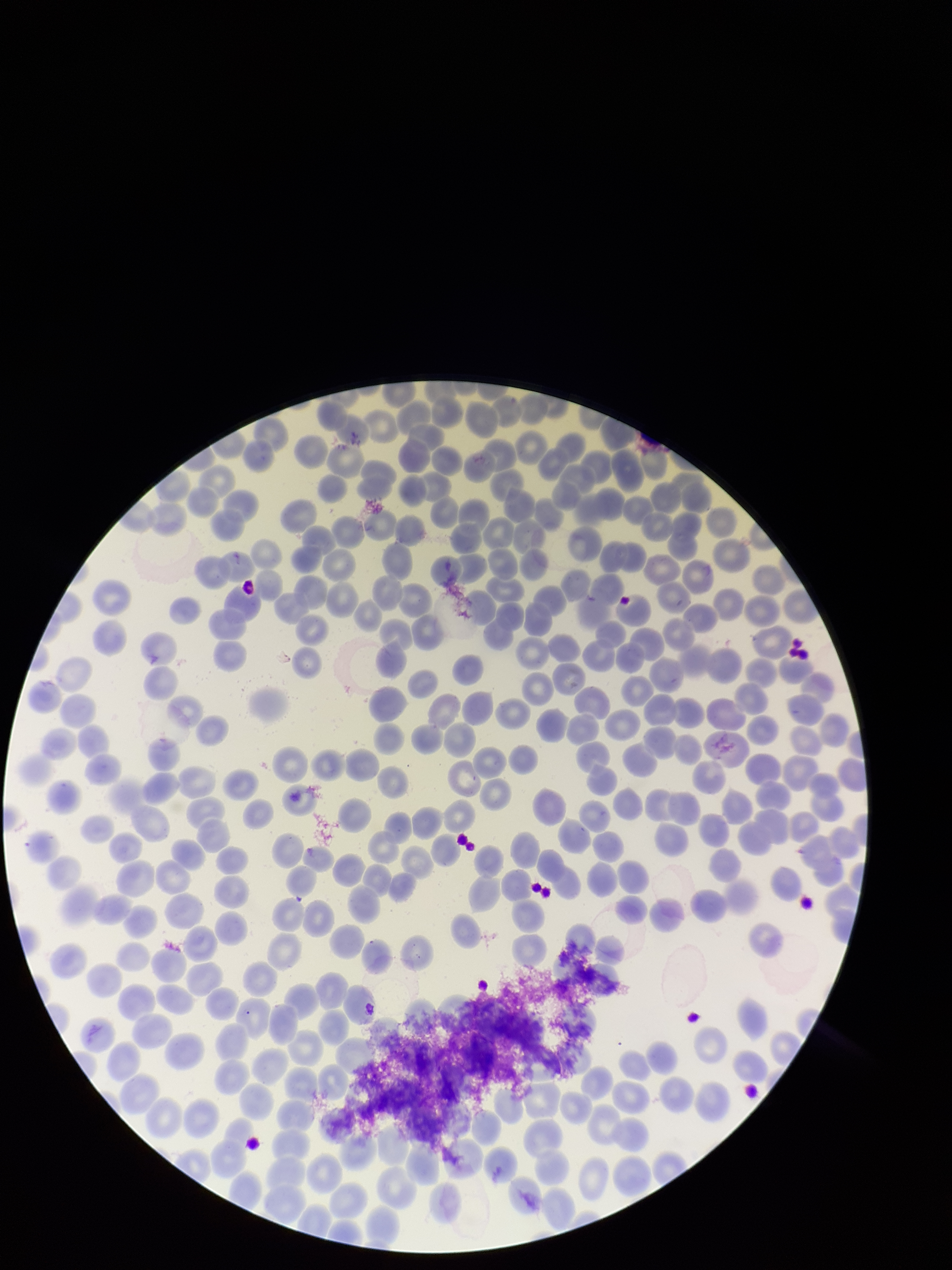

Photographed through the microscope eyepiece with a smartphone camera. Parasitized red blood cell count: 0. Preparation: thin blood smear. Patient malaria status: positive. Red blood cell count: 248. One field from this slide. Parasitized red blood cells: none identified. Species reported for this patient: Plasmodium vivax. Image is 952×1270 pixels. Giemsa stain.